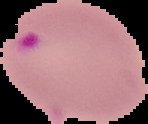 Image is 148×124 pixels. The area outside the segmented cell region is set to black. From a thin blood smear. Result: malaria parasites identified.